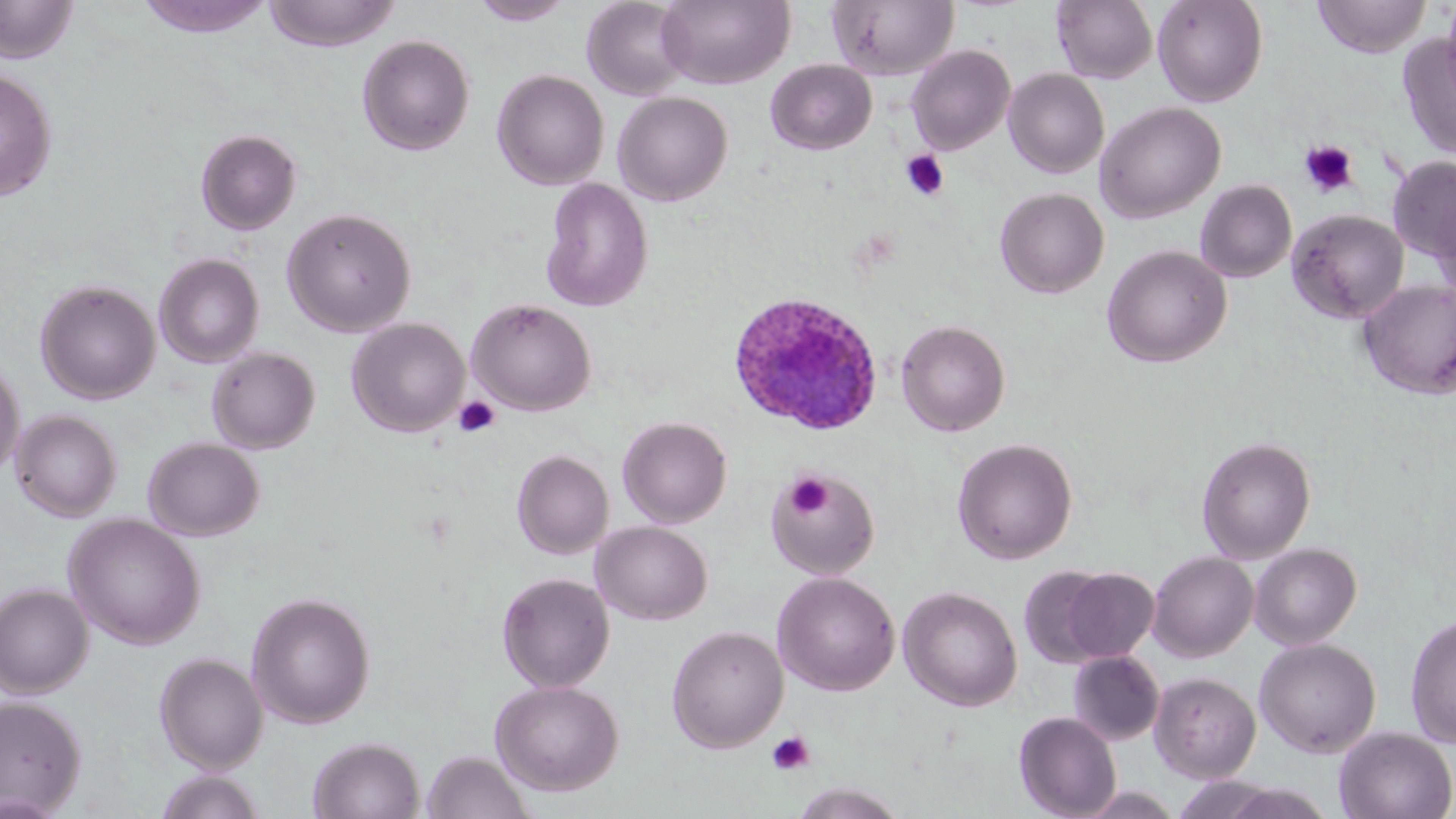 Approximate bounding boxes as [x1, y1, x2, y2] in pixels. Uninfected red blood cell locations: [0, 0, 79, 63], [134, 0, 278, 38], [262, 0, 401, 51], [470, 0, 574, 25], [582, 0, 692, 101], [656, 0, 795, 89], [827, 0, 960, 81], [1051, 0, 1157, 84], [1152, 0, 1268, 107], [1313, 0, 1430, 57], [1440, 0, 1456, 106], [1397, 32, 1456, 161], [356, 34, 474, 155], [906, 44, 1015, 155], [766, 59, 877, 154], [0, 68, 57, 202], [492, 69, 610, 190], [1004, 69, 1109, 178], [493, 81, 733, 195], [613, 91, 733, 206], [1095, 101, 1225, 223], [195, 128, 302, 235], [1388, 155, 1456, 268], [540, 177, 654, 312], [1195, 179, 1296, 283], [995, 187, 1109, 298], [1431, 192, 1456, 307], [281, 207, 416, 337], [1287, 209, 1409, 324], [1101, 244, 1232, 368], [153, 253, 264, 368], [35, 279, 161, 404], [1358, 280, 1456, 400], [468, 299, 596, 416], [347, 318, 470, 437], [896, 319, 1010, 436], [206, 347, 320, 454], [0, 356, 25, 484], [10, 410, 121, 522], [617, 416, 732, 528], [1197, 435, 1316, 563], [143, 437, 265, 541], [952, 437, 1078, 565], [512, 450, 613, 559], [766, 468, 880, 580], [64, 514, 206, 650], [591, 521, 713, 624], [1250, 543, 1362, 650], [1148, 551, 1258, 661], [1018, 566, 1118, 668], [1059, 568, 1159, 662], [773, 571, 900, 696], [497, 572, 615, 692], [0, 583, 93, 698], [898, 586, 1022, 712], [246, 591, 376, 728], [1404, 614, 1456, 748], [666, 625, 788, 752], [1254, 638, 1381, 757], [1067, 650, 1164, 746], [154, 652, 268, 772], [1150, 672, 1261, 783], [490, 679, 624, 796], [0, 695, 87, 816], [1014, 711, 1122, 819], [1334, 727, 1456, 819], [308, 736, 426, 819], [421, 749, 535, 819], [154, 770, 267, 819], [789, 782, 909, 819]. Plasmodium ovale-infected red blood cell locations: [727, 291, 884, 437]. Platelet locations: [1298, 140, 1360, 198], [901, 150, 949, 201], [454, 396, 501, 438], [786, 473, 832, 518], [767, 731, 816, 776]. Slide-level diagnosis: Plasmodium ovale. Optical microscopy. Image is 1456×819 pixels. May-Grünwald-Giemsa-stained preparation. Single field of view. Captured at 1000x magnification. Thin blood smear.